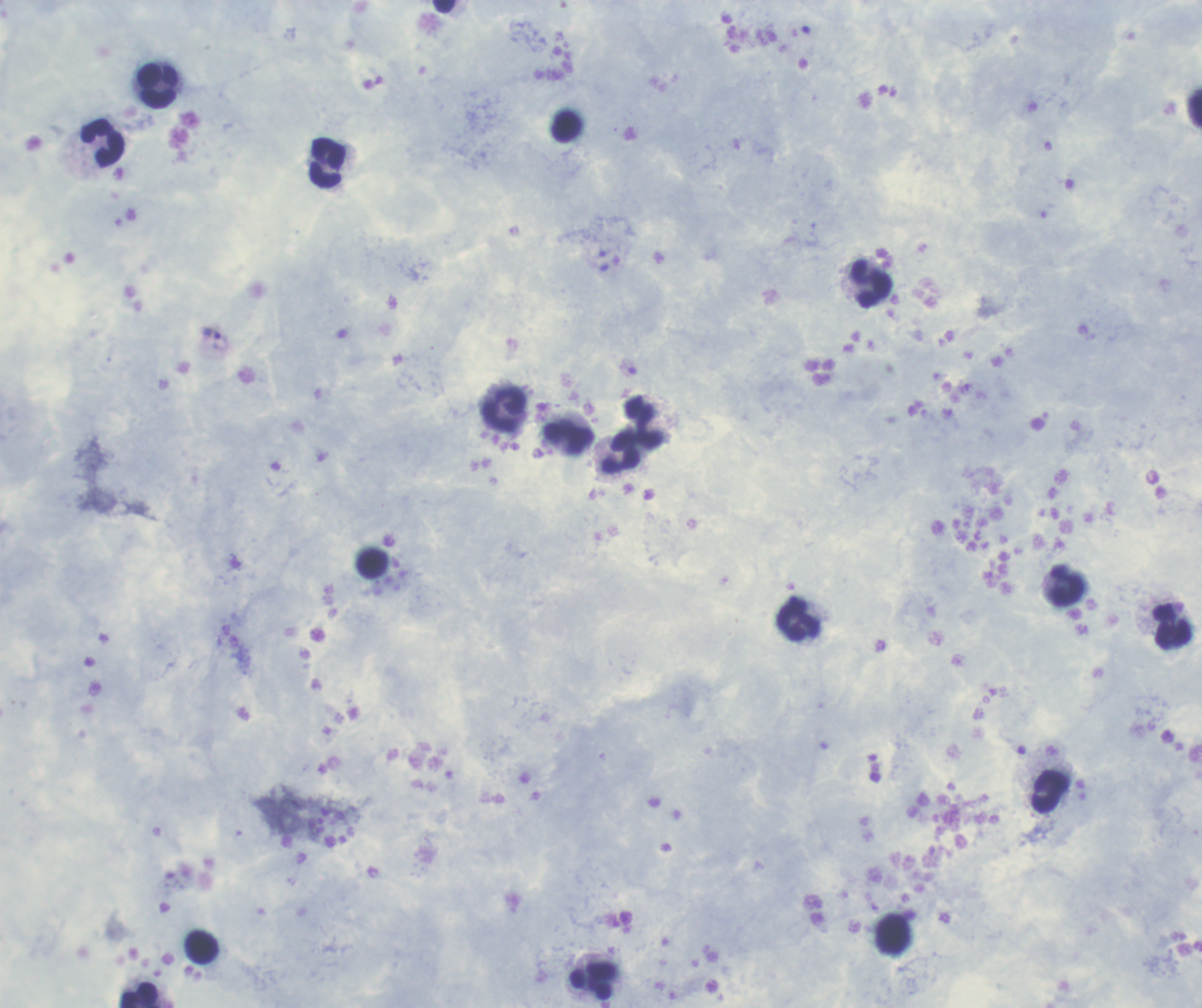

Coloration quality: good. Single field of view. Romanowsky stain. Thick blood film. Image is 1202×1008 pixels.